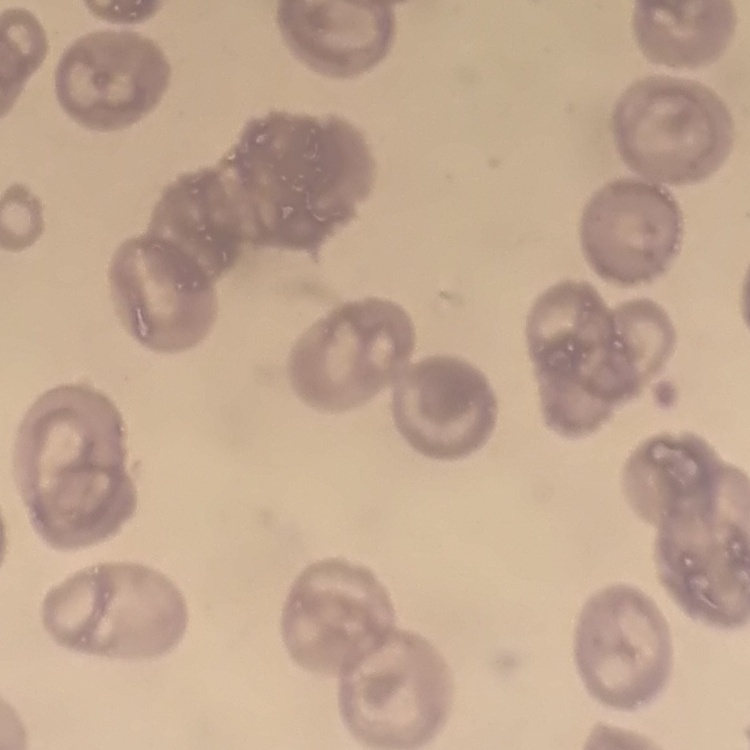

Summary:
  - Erythrocyte morphology: no rouleaux formation
  - Preparation: thin blood film
  - Image type: one tile cut from a larger photomicrograph
  - Stain: Field's or Giemsa